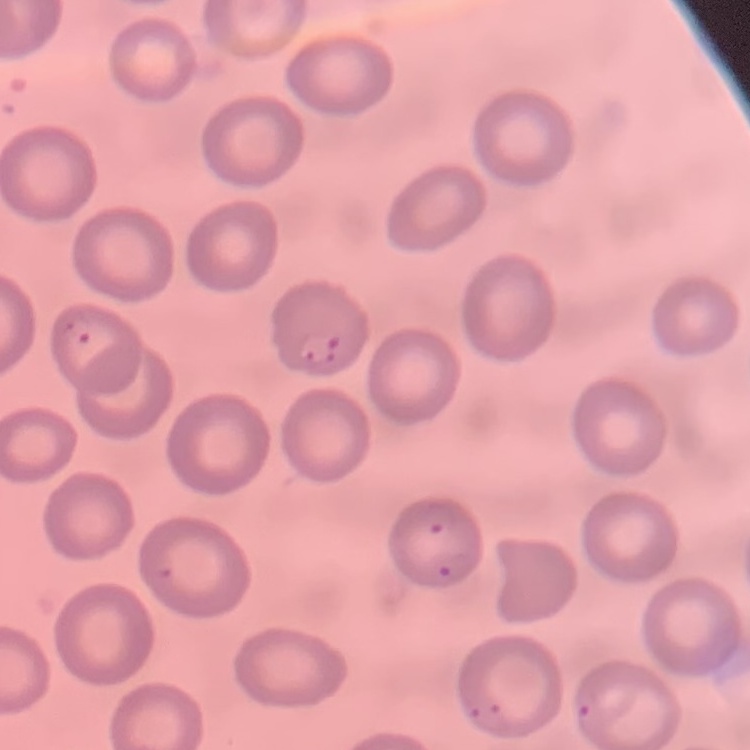
erythrocyte morphology = no rouleaux formation
stain = Field's or Giemsa
image type = one tile cut from a larger photomicrograph
preparation = thin blood smear